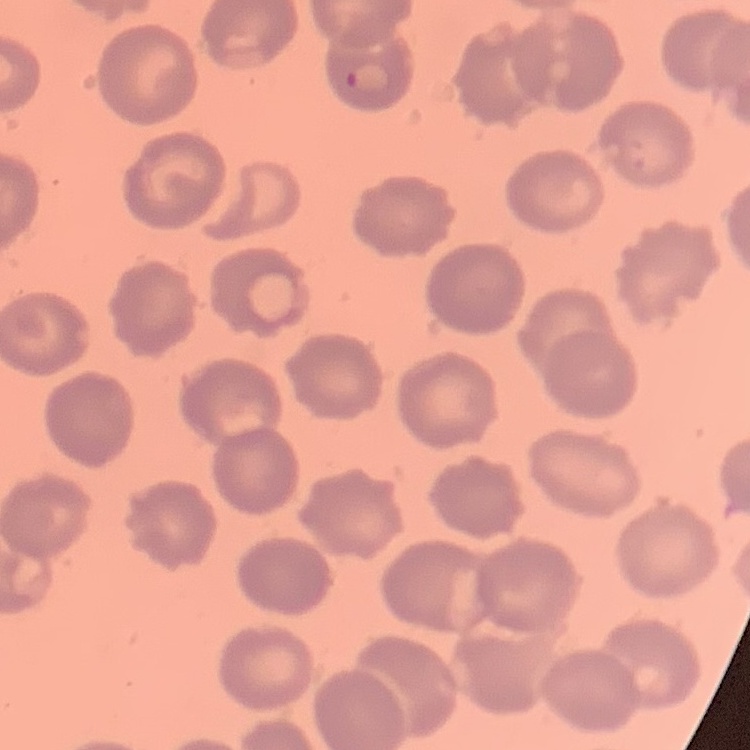
Summary:
  - Erythrocyte morphology: no rouleaux formation
  - Preparation: thin blood smear
  - Image type: one tile cut from a larger photomicrograph
  - Stain: Field's or Giemsa